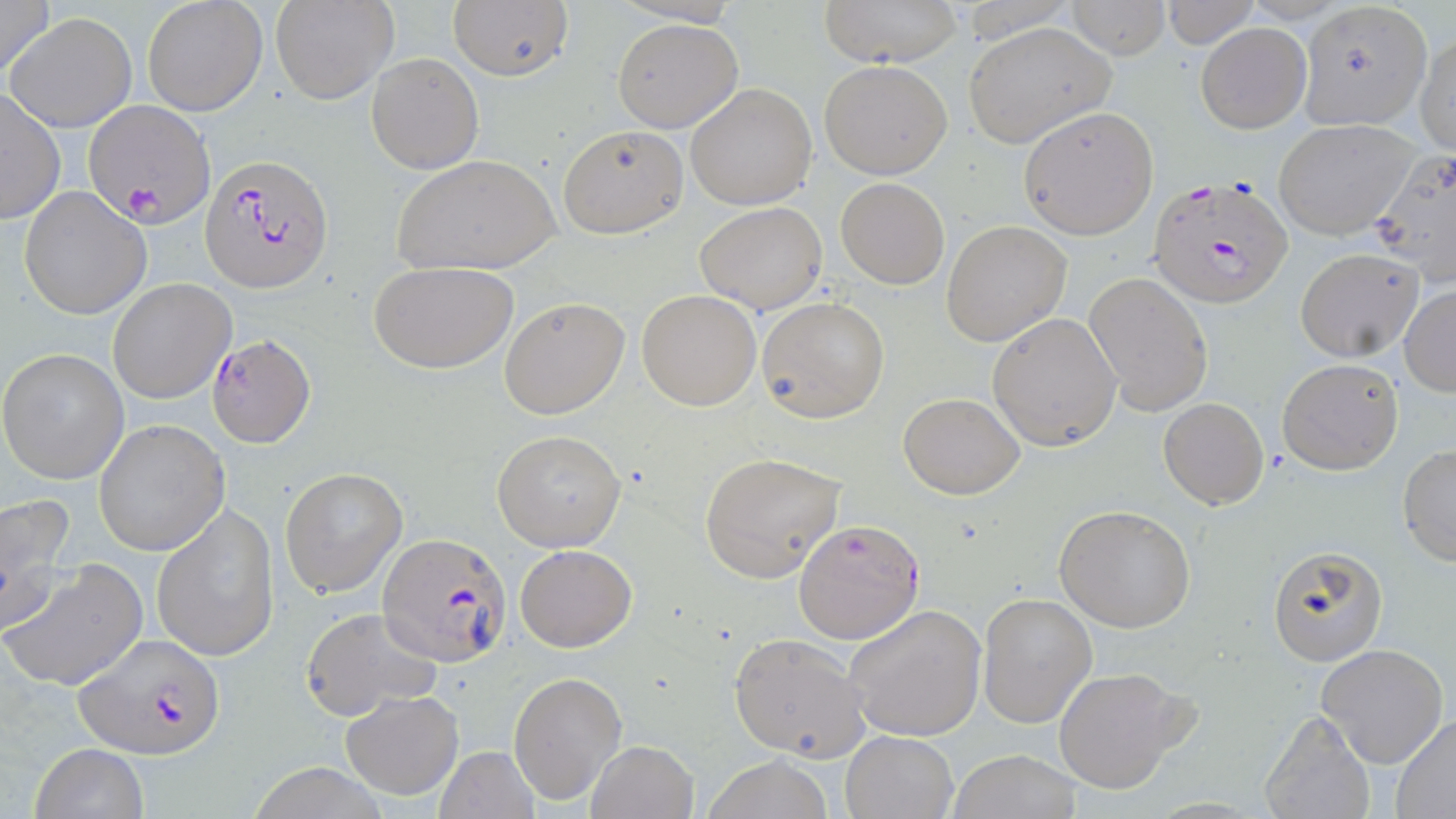 Approximate bounding boxes as (x1,y1)-(x2,y2) corner pairs in pixels. Plasmodium falciparum-infected red blood cell locations: (86,104)-(212,220), (201,154)-(334,291), (1147,173)-(1293,309), (205,333)-(315,446), (378,530)-(511,667), (77,634)-(225,759). Uninfected red blood cell locations: (0,0)-(55,86), (142,0)-(267,118), (821,0)-(961,66), (269,1)-(397,105), (449,1)-(573,82), (1159,1)-(1262,47), (1300,1)-(1435,129), (1062,2)-(1170,60), (7,12)-(137,133), (612,19)-(743,133), (964,21)-(1116,148), (1196,22)-(1311,133), (1415,32)-(1455,156), (366,53)-(484,174), (818,59)-(951,179), (685,83)-(818,210), (0,87)-(65,225), (1017,107)-(1159,240), (1273,119)-(1419,240), (557,125)-(688,239), (1369,146)-(1456,286), (391,152)-(561,276), (835,177)-(949,288), (19,185)-(150,320), (694,201)-(827,315), (941,220)-(1073,348), (1294,247)-(1424,361), (367,260)-(519,374), (1084,270)-(1213,415), (107,278)-(236,404), (1400,285)-(1456,394), (637,290)-(762,410), (758,296)-(890,424), (499,297)-(629,419), (988,312)-(1120,450), (0,348)-(130,484), (1277,357)-(1404,474), (898,392)-(1024,499), (1158,397)-(1269,509), (93,419)-(230,557), (494,429)-(625,551), (1398,446)-(1456,566), (699,453)-(846,583), (280,465)-(407,596), (1,495)-(77,634), (1055,505)-(1195,633), (151,507)-(278,660), (794,518)-(924,644), (515,544)-(637,652), (1270,547)-(1388,666), (3,558)-(147,693), (976,592)-(1097,728), (843,602)-(988,742), (298,606)-(445,725), (729,632)-(871,761), (1316,643)-(1449,769), (1053,666)-(1194,795), (509,671)-(627,805), (341,690)-(463,800), (1259,709)-(1377,819), (1390,714)-(1456,816), (841,730)-(957,819), (586,739)-(698,819), (31,743)-(147,819), (434,745)-(540,819), (946,750)-(1082,818), (701,755)-(837,819), (242,765)-(389,819). Slide-level diagnosis: Plasmodium falciparum. Single field of view. Light microscopy. Captured at 1000x magnification. Thin blood film. Image is 1456×819 pixels. May-Grünwald-Giemsa stain.